Comment on the morphology of the erythrocytes.
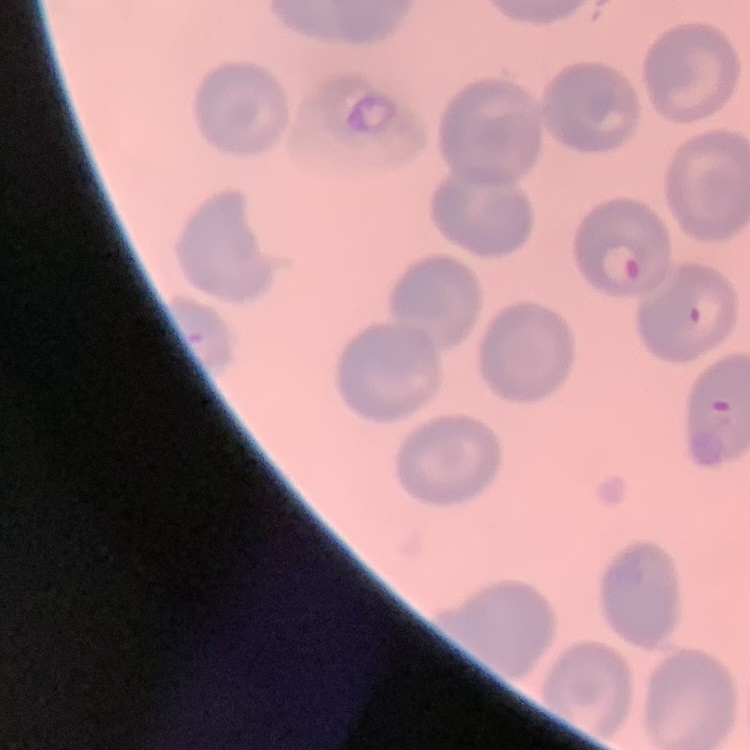

No rouleaux formation.

Stained with either Field's or Giemsa. One tile cut from a larger photomicrograph. Thin blood film.